Classify this cell by malaria status.
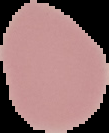
Uninfected.

preparation = thin blood smear
image type = segmented cell region with the area outside set to black
image size = 109×133 pixels